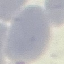

malaria_status: uninfected
capture: smartphone through the microscope eyepiece
preparation: thin blood film
stain: Giemsa
image_type: cell patch, automatically extracted from a larger field of view and resized to 64 × 64 pixels